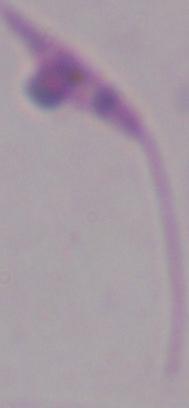 1000x magnification. A Leishmania parasite is shown. Micrograph.